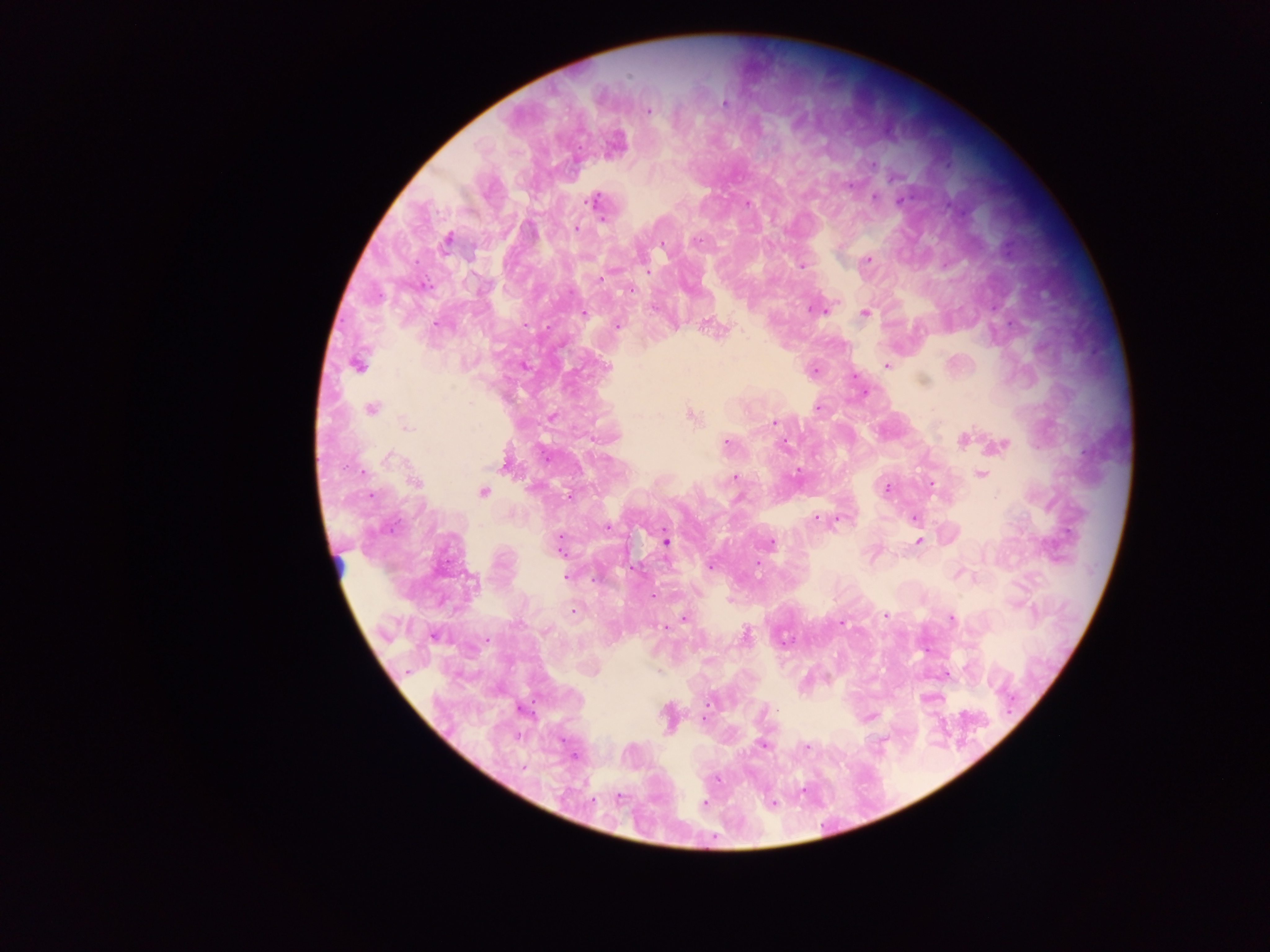
{
  "field_of_view": "single",
  "image_size": "1270×952 pixels",
  "preparation": "thick blood smear",
  "country": "Ghana",
  "capture": "mobile-phone photograph through a microscope",
  "malaria_parasite_locations": "approximate centers as (x, y) in pixels: (628, 78), (724, 102), (647, 110), (875, 165), (849, 186), (876, 197), (594, 201), (900, 201), (749, 204), (575, 227), (446, 240), (664, 246), (867, 259), (803, 266), (647, 271), (600, 280), (623, 289), (865, 312), (581, 313), (705, 320), (436, 323), (618, 325), (721, 332), (357, 364), (887, 366), (607, 367), (815, 369), (922, 380), (371, 408), (819, 408), (690, 418), (771, 422), (964, 439), (784, 443), (726, 445), (996, 448), (506, 467), (362, 472), (798, 474), (980, 474), (736, 477), (932, 482), (886, 487), (483, 493), (566, 493), (916, 517), (815, 519), (608, 526), (916, 540), (666, 542), (770, 543), (559, 547), (710, 566), (757, 573), (956, 574), (566, 575), (974, 577), (574, 611), (884, 615), (683, 618), (952, 619), (844, 623), (664, 628), (545, 631), (434, 635), (488, 638), (830, 680), (708, 702), (704, 715), (761, 746), (622, 797), (702, 802)"
}